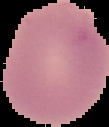 Image is 109×127 pixels. Result: no Plasmodium parasites seen. From a thin blood smear. Segmented cell region on a black background.